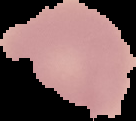

{
  "image_size": "136×121 pixels",
  "preparation": "thin blood smear",
  "image_type": "cell region segmented out of the field of view; surrounding area masked to black",
  "result": "no Plasmodium parasites seen"
}